Report the malaria status of this cell.
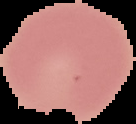
Uninfected.

Image is 136×124 pixels. Cell region segmented out of the field of view; the surrounding area is masked to black. From a thin blood smear.